Classify this cell by malaria status.
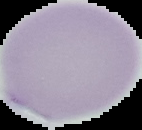

Uninfected.

preparation = thin blood film
image type = segmented cell region with the area outside set to black
image size = 142×130 pixels